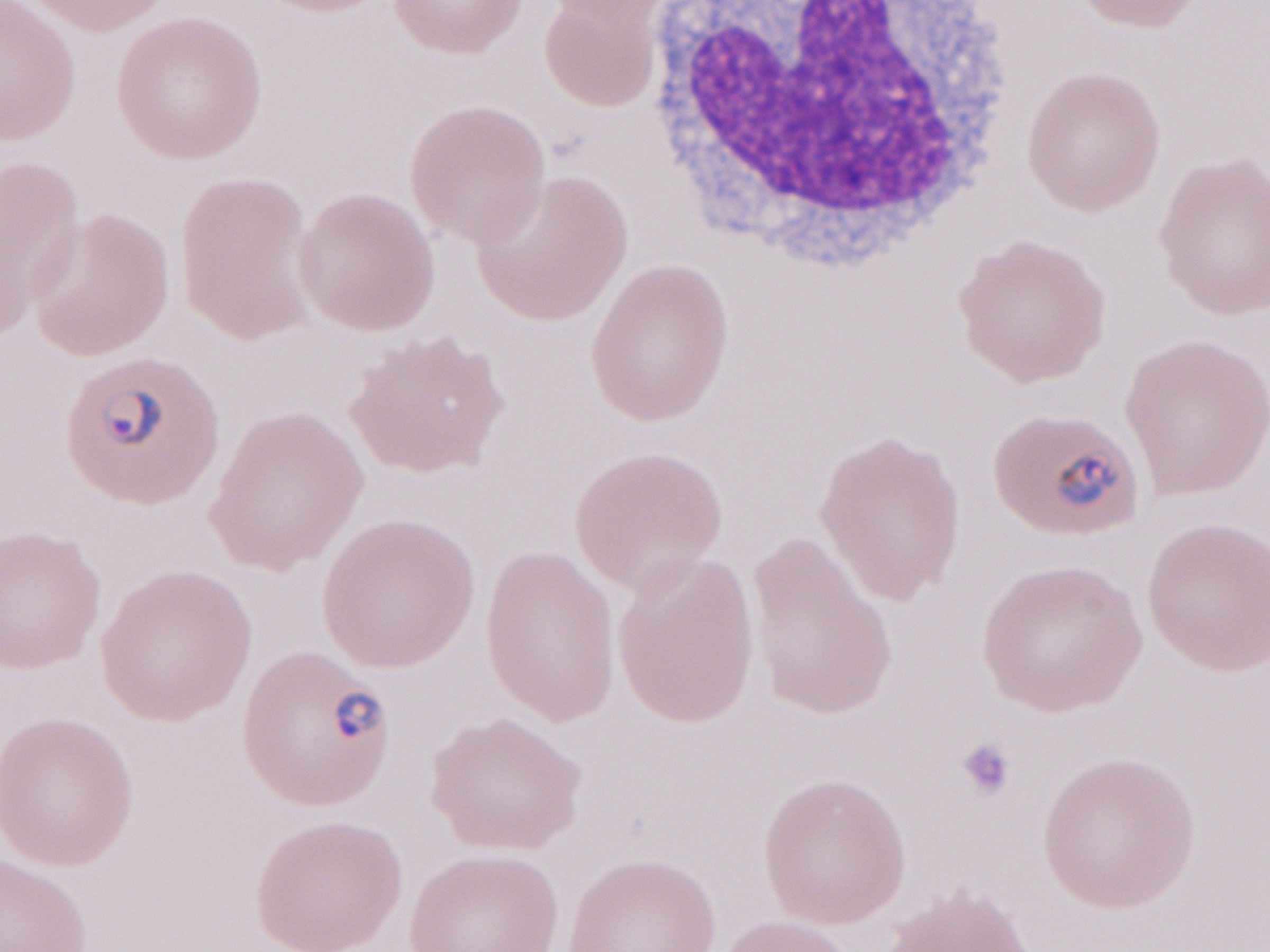
Image is 1270×952 pixels. Olympus BX43 microscope and DP73 digital camera. Thin blood smear. Patient diagnosis: malaria infection. Magnification: 1,000x. Single field of view. May-Grünwald-Giemsa stain.